Name the blood parasite species.
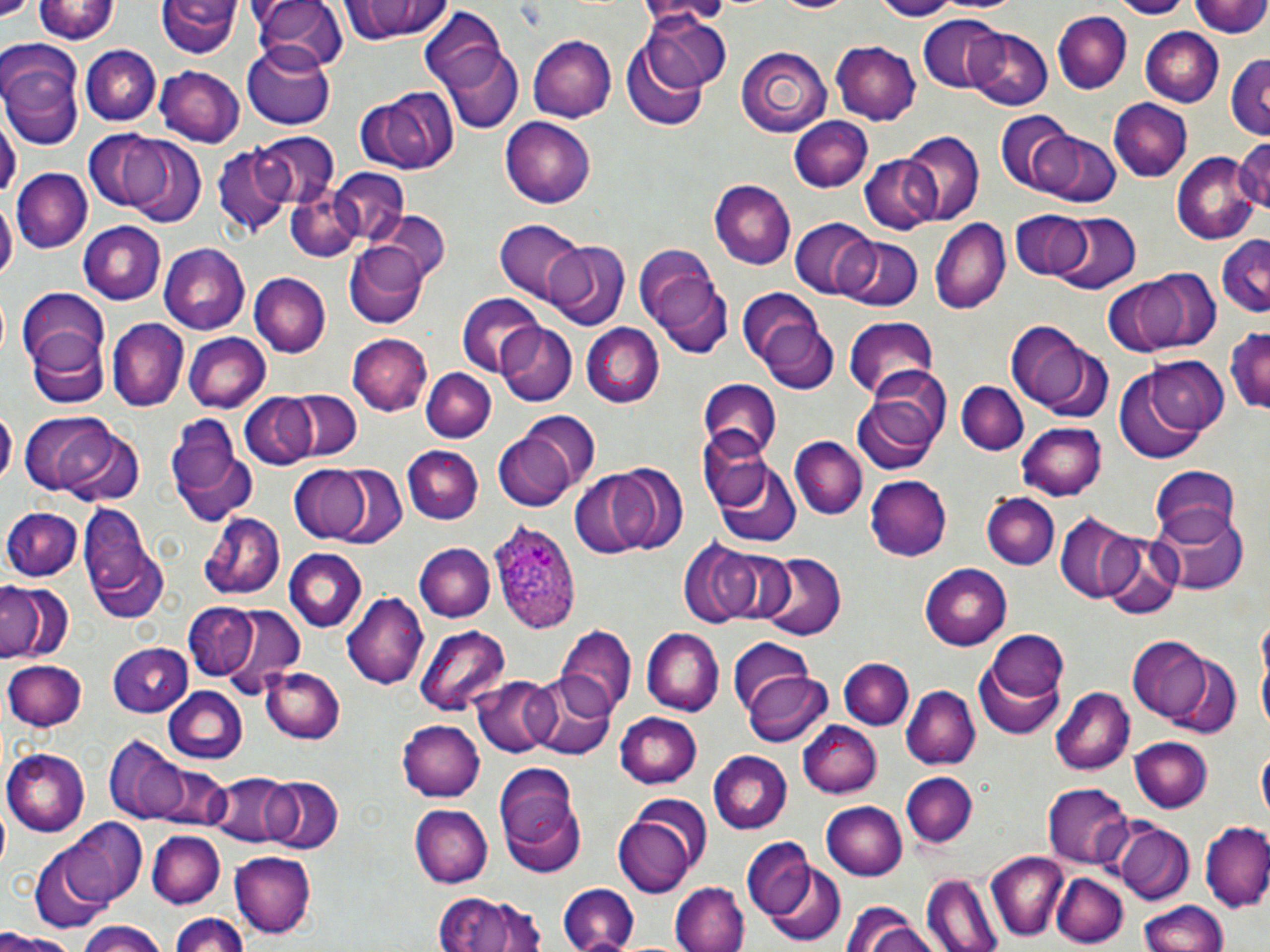

Plasmodium ovale.

preparation = thin blood film
uninfected red blood cell locations = approximate bounding boxes as (x1, y1, x2, y2) in pixels: (33, 0, 120, 45), (340, 0, 456, 44), (771, 0, 856, 15), (868, 0, 959, 20), (1116, 0, 1188, 18), (1193, 0, 1270, 39), (157, 1, 240, 59), (251, 1, 343, 73), (420, 10, 510, 99), (1055, 11, 1131, 94), (641, 12, 732, 93), (918, 15, 1009, 93), (1140, 27, 1224, 105), (966, 28, 1052, 110), (528, 35, 616, 121), (621, 43, 708, 131), (831, 43, 923, 125), (81, 44, 159, 126), (241, 44, 337, 130), (1, 45, 85, 148), (440, 45, 522, 135), (737, 47, 833, 132), (1227, 51, 1270, 142), (155, 65, 245, 146), (355, 88, 459, 175), (1107, 99, 1193, 182), (0, 109, 18, 208), (993, 112, 1080, 196), (789, 116, 873, 192), (501, 117, 596, 209), (256, 131, 338, 208), (901, 132, 983, 224), (1041, 132, 1120, 206), (84, 133, 166, 213), (1232, 137, 1270, 217), (122, 140, 208, 229), (211, 145, 291, 237), (1172, 153, 1258, 245), (860, 156, 938, 234), (330, 168, 411, 246), (16, 169, 92, 252), (708, 182, 795, 270), (286, 188, 363, 261), (0, 203, 14, 285), (374, 210, 451, 287), (1010, 211, 1094, 280), (1051, 212, 1139, 292), (931, 218, 1011, 311), (790, 219, 880, 299), (497, 221, 587, 304), (76, 223, 166, 305), (1216, 235, 1270, 318), (836, 237, 923, 312), (549, 241, 629, 329), (160, 244, 248, 333), (632, 244, 724, 343), (344, 245, 428, 329), (1137, 268, 1219, 351), (250, 273, 332, 356), (652, 275, 733, 358), (1101, 277, 1185, 357), (738, 288, 832, 381), (16, 290, 109, 367), (455, 295, 546, 377), (843, 318, 939, 400), (106, 320, 188, 411), (1005, 321, 1100, 416), (1226, 322, 1270, 414), (497, 323, 578, 405), (582, 324, 664, 407), (28, 332, 109, 408), (348, 332, 432, 415), (183, 333, 270, 413), (1142, 356, 1230, 435), (419, 369, 493, 443), (1117, 371, 1207, 463), (699, 378, 781, 459), (956, 380, 1028, 454), (851, 387, 944, 477), (285, 390, 361, 460), (240, 393, 316, 469), (0, 406, 19, 490), (20, 412, 121, 496), (518, 412, 602, 496), (168, 417, 254, 521), (1017, 424, 1105, 500), (55, 428, 144, 507), (492, 431, 579, 511), (696, 431, 773, 512), (790, 437, 867, 519), (399, 446, 482, 525), (712, 459, 801, 549), (288, 466, 370, 543), (1150, 466, 1243, 543), (568, 471, 661, 561), (865, 477, 951, 560), (984, 493, 1058, 568), (77, 501, 161, 617), (1151, 504, 1249, 595), (4, 507, 84, 581), (200, 513, 284, 599), (1054, 513, 1143, 604), (1100, 534, 1180, 619), (677, 536, 767, 629), (413, 543, 494, 623), (711, 546, 797, 627), (283, 550, 366, 632), (758, 552, 845, 641), (920, 565, 1010, 651), (0, 581, 69, 664), (342, 592, 428, 690), (181, 603, 261, 679), (212, 606, 306, 694), (416, 625, 511, 715), (556, 628, 636, 721), (643, 628, 724, 715), (978, 631, 1069, 735), (1129, 637, 1216, 723), (726, 640, 813, 718), (107, 644, 195, 716), (4, 659, 86, 732), (841, 659, 912, 730), (262, 666, 344, 743), (743, 670, 832, 747), (527, 673, 616, 757), (472, 675, 558, 756), (162, 686, 247, 763), (900, 686, 981, 769), (1052, 687, 1135, 775), (613, 711, 703, 789), (396, 718, 485, 801), (798, 720, 881, 798), (1129, 734, 1212, 813), (107, 737, 193, 825), (1258, 745, 1269, 828), (3, 749, 91, 835), (708, 751, 792, 833), (497, 763, 586, 875), (901, 771, 978, 849), (206, 773, 298, 847), (261, 776, 342, 852), (1043, 783, 1132, 867), (821, 799, 907, 880), (410, 804, 492, 888), (615, 813, 700, 899), (56, 820, 144, 904), (1112, 821, 1194, 902), (1201, 823, 1270, 914), (147, 829, 224, 908), (742, 840, 814, 918), (29, 849, 112, 934), (231, 851, 316, 940), (987, 854, 1067, 941), (761, 857, 845, 946), (1053, 873, 1126, 946), (921, 875, 1002, 952), (671, 882, 748, 952), (557, 885, 638, 952), (432, 890, 549, 952), (1139, 901, 1229, 952), (170, 913, 251, 952), (844, 913, 947, 952), (76, 924, 169, 952), (0, 932, 79, 952)
modality = light microscopy
image size = 1270×952 pixels
platelet locations = approximate bounding boxes as (x1, y1, x2, y2) in pixels: (0, 0, 31, 17)
field of view = one of a larger specimen
Plasmodium ovale-infected red blood cell locations = approximate bounding boxes as (x1, y1, x2, y2) in pixels: (489, 519, 581, 636)
magnification = 1000x
stain = May-Grünwald-Giemsa